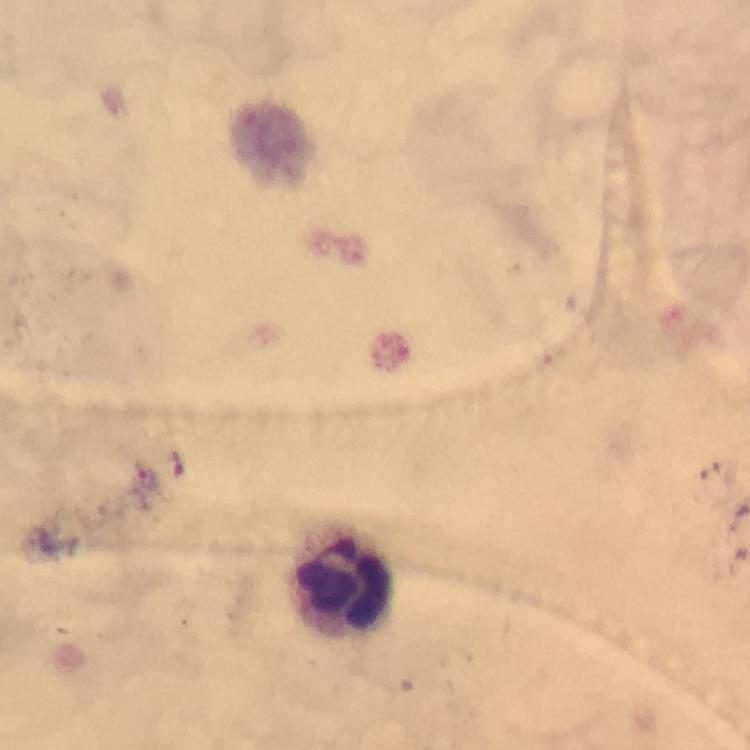
Plasmodium parasite locations = approximate centers as [x, y] in pixels: [147, 479]
leukocyte locations = approximate centers as [x, y] in pixels: [340, 579]
immersion oil = used
image size = 750×750 pixels
context = from a diagnostic examination for malaria
capture = smartphone camera through the microscope
cropped from = a single field of view
magnification = 100x
stain = Giemsa
preparation = thick smear